Name the parasite shown.
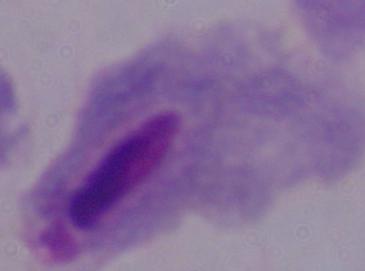

A trichomonad.

Summary:
  - Magnification: 1000x
  - Modality: micrograph